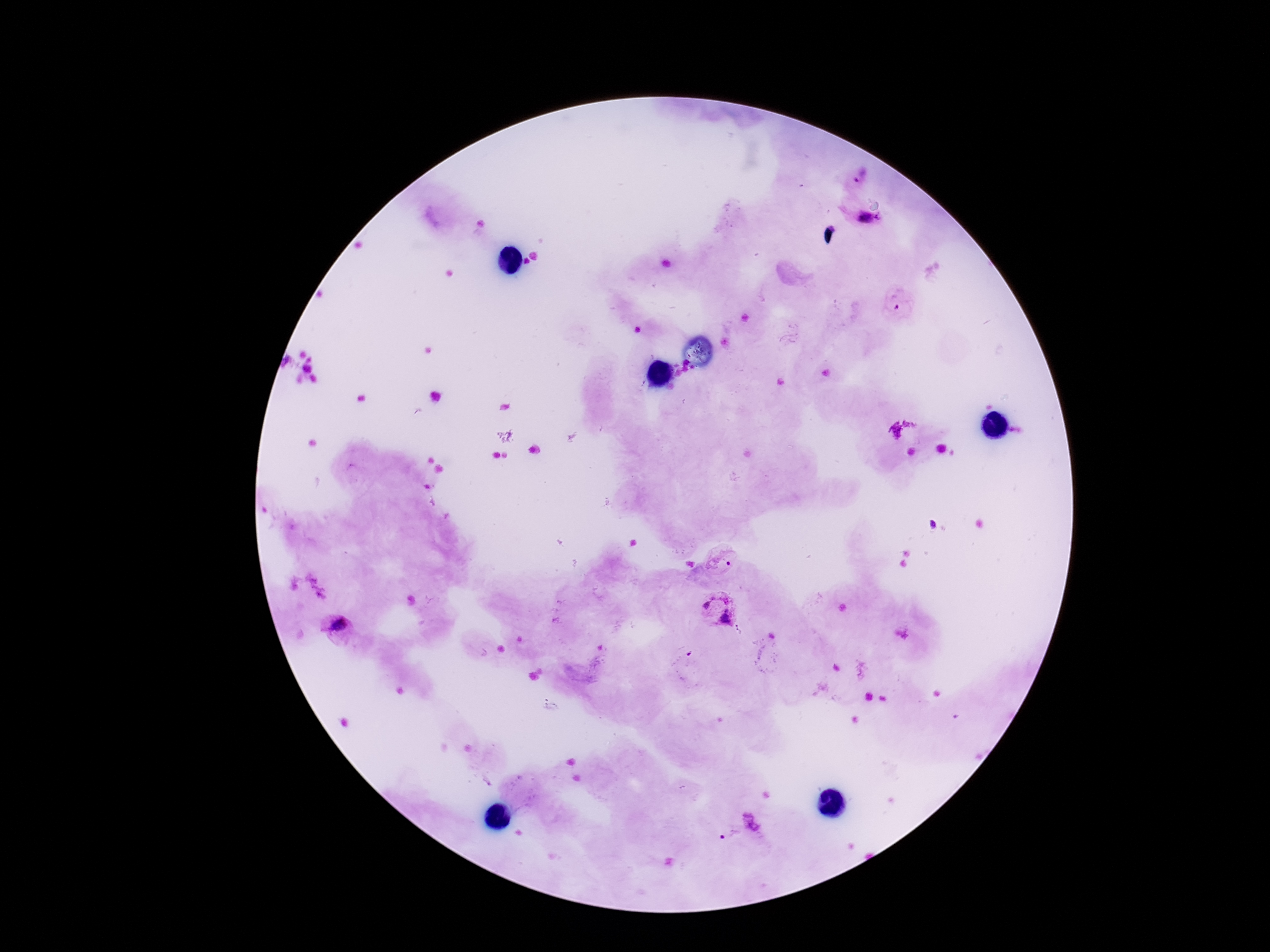 Approximate centers as {x, y} in pixels. Plasmodium parasite locations: {861, 175}, {866, 221}, {901, 298}, {720, 562}, {718, 609}, {339, 635}, {683, 659}, {755, 822}, {731, 836}. Single field of view. Patient malaria status: infected. Photographed through the microscope eyepiece with a smartphone camera. Image is 1270×952 pixels. Thick blood film. Giemsa-stained preparation. 100x magnification.